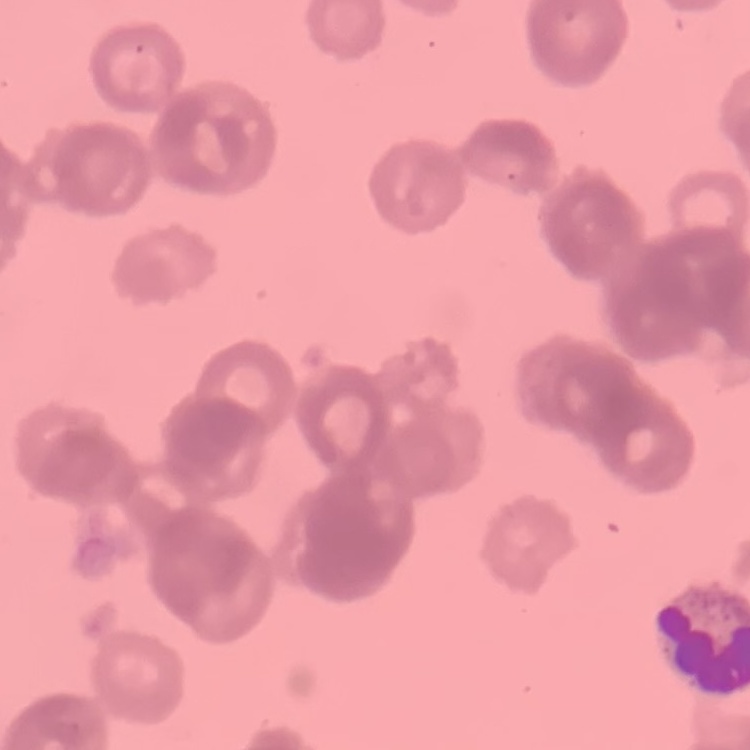

red blood cell morphology = rouleaux formation
image type = square crop of a larger photomicrograph
preparation = thin blood smear
stain = Field's or Giemsa